Assess this cell for malaria.
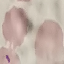

Parasitized.

Giemsa-stained preparation. Cell patch, automatically extracted from a larger field of view and resized to 64 × 64 pixels. Acquired by smartphone through the microscope eyepiece. Thin smear of blood.